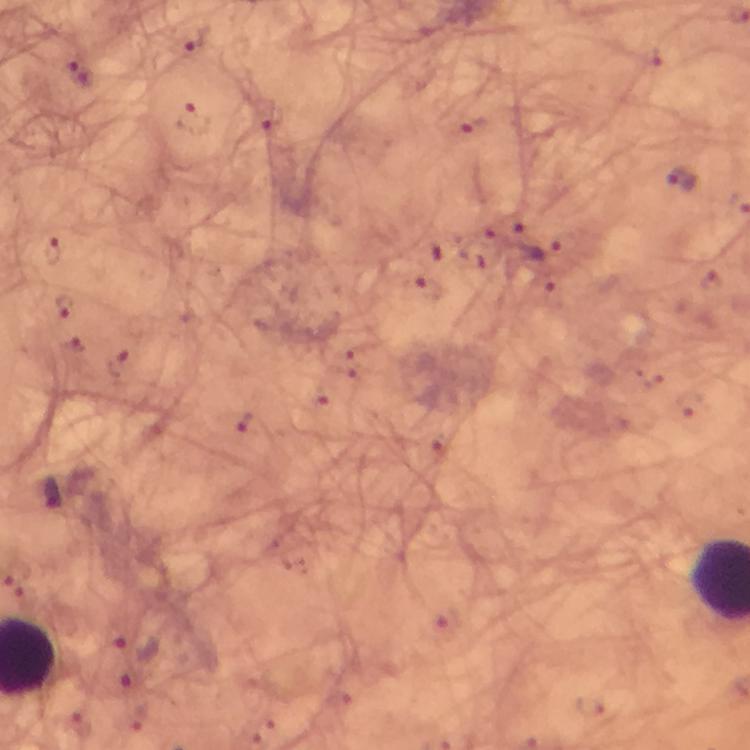

Approximate centers as (x, y) in pixels. Malaria parasite locations: (79, 73), (192, 118), (475, 128), (681, 181), (513, 226), (447, 248), (543, 250), (52, 251), (67, 307), (75, 345), (117, 364), (54, 492), (446, 620), (115, 636), (82, 723). A crop from one field of view. Giemsa stain. Thick blood smear. Image is 750×750 pixels. From a diagnostic examination for malaria. Smartphone photograph taken through a microscope. 100x magnification. Immersion oil applied.